Outline each uninfected red blood cell.
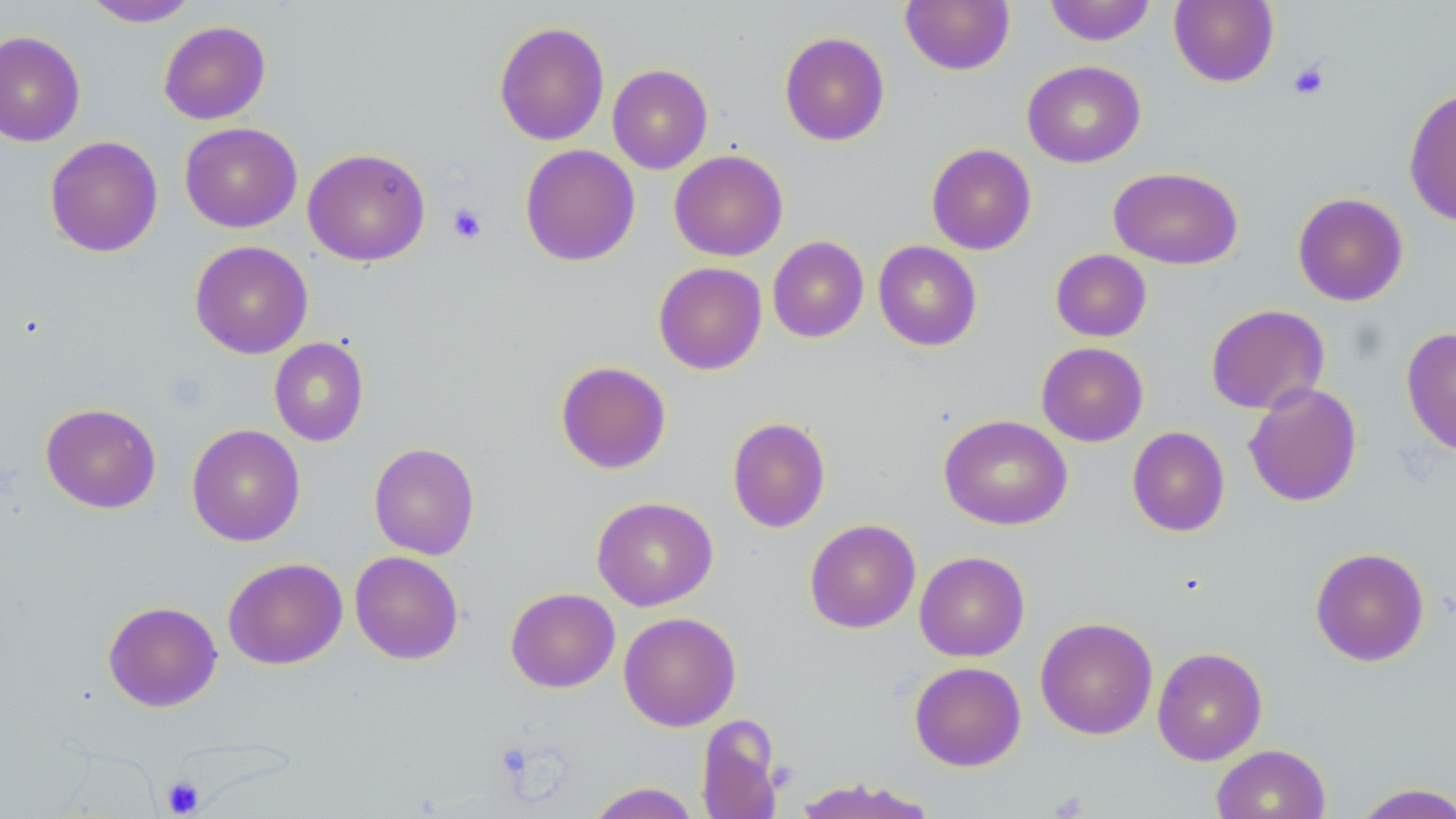
Approximate bounding boxes as (x1,y1)-(x2,y2) corner pairs in pixels.
Uninfected red blood cells: (82,0)-(201,27), (900,0)-(1015,75), (1043,0)-(1157,45), (1168,0)-(1279,87), (158,21)-(271,125), (494,21)-(610,146), (0,31)-(85,147), (779,31)-(890,146), (1022,60)-(1146,168), (607,64)-(713,174), (1403,86)-(1456,227), (179,122)-(302,233), (44,135)-(163,257), (926,143)-(1037,255), (519,144)-(640,267), (303,147)-(430,266), (669,150)-(788,261), (1108,166)-(1244,270), (1292,192)-(1408,306), (767,236)-(868,343), (189,240)-(313,359), (873,240)-(982,351), (1050,249)-(1152,342), (653,262)-(767,375), (1205,304)-(1330,415), (1401,327)-(1456,457), (268,337)-(369,447), (1036,342)-(1149,446), (555,361)-(671,474), (1243,382)-(1362,507), (40,403)-(162,514), (938,414)-(1072,530), (727,416)-(831,533), (187,424)-(305,546), (1127,426)-(1230,536), (368,442)-(480,560), (591,496)-(718,611), (804,519)-(921,634), (1310,547)-(1430,666), (349,551)-(464,664), (914,551)-(1030,662), (223,557)-(348,670), (505,587)-(620,693), (103,601)-(222,712), (618,612)-(741,731), (1035,617)-(1158,740), (1152,647)-(1267,765), (909,661)-(1027,771), (696,715)-(784,819), (1211,744)-(1331,819), (792,777)-(940,818), (586,782)-(700,819), (1351,783)-(1456,819).

Platelet locations: (1287,60)-(1330,100), (447,202)-(488,245), (161,775)-(204,816). Slide-level diagnosis: negative for blood parasites. Thin blood smear. Image is 1456×819 pixels. Light microscopy. 1000x magnification. May-Grünwald-Giemsa stain. One field of a larger specimen.